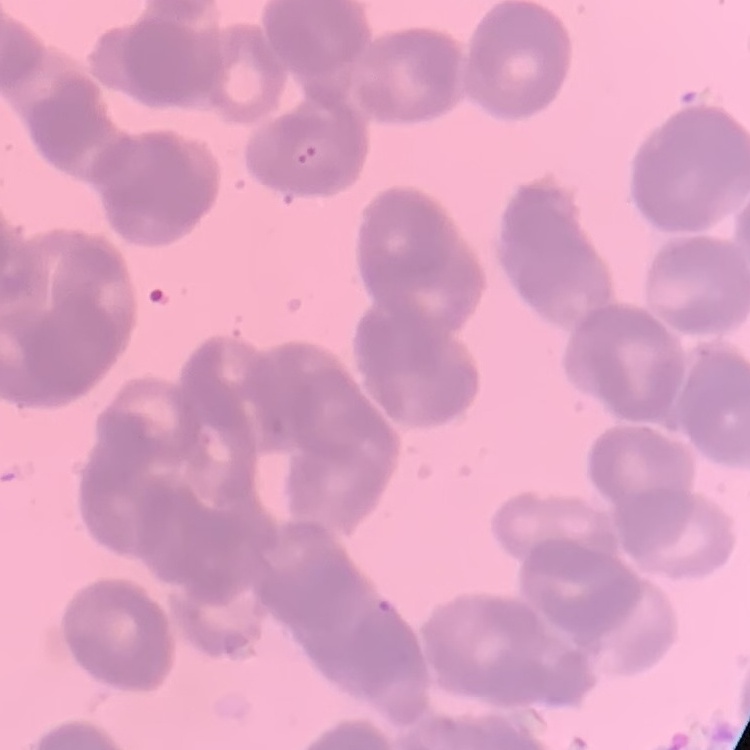
erythrocyte morphology = rouleaux formation
stain = Field's or Giemsa
image type = square crop of a larger photomicrograph
preparation = thin blood film